Describe the morphology of the red blood cells.
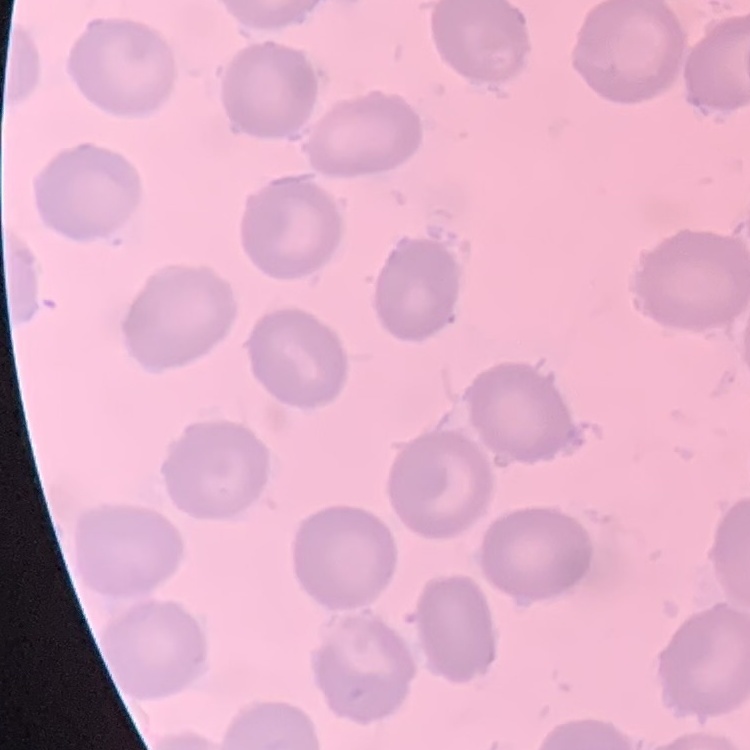
No rouleaux formation.

Thin blood film. Field's or Giemsa stain. Square crop of a larger photomicrograph.